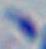

modality: micrograph
magnification: 1000x
identification: Toxoplasma gondii